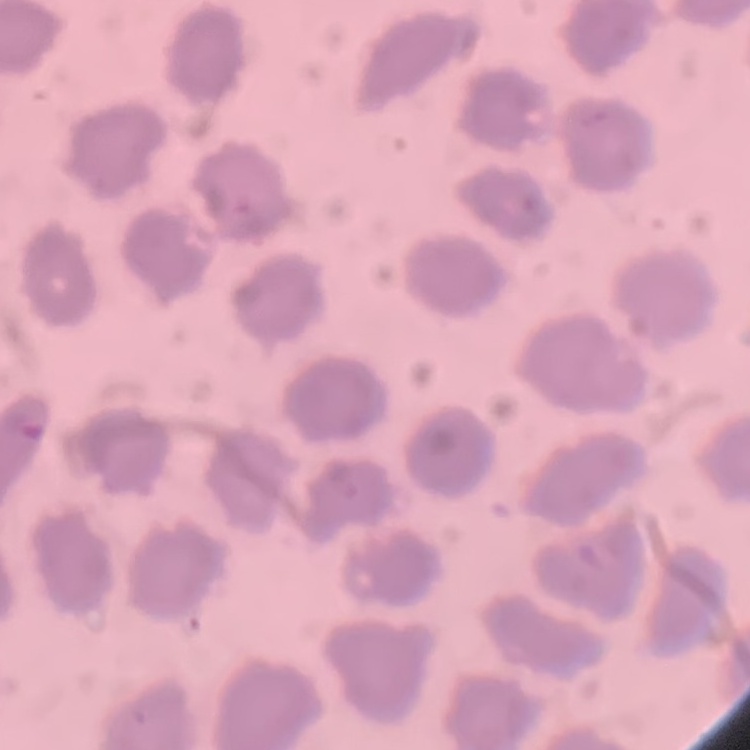 The erythrocytes exhibit no rouleaux formation. Field's or Giemsa stain. Thin blood film. Square crop of a larger photomicrograph.